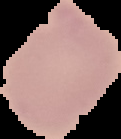

image type = cell region segmented out of the field of view; surrounding area masked to black
preparation = thin blood smear
image size = 121×139 pixels
malaria status = uninfected